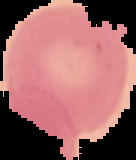 The area outside the segmented cell region is set to black. From a thin blood smear. Result: negative for Plasmodium parasites. Image is 136×160 pixels.